Identify the parasite.
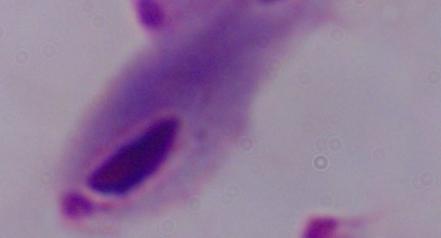
A trichomonad.

Captured at 1000x magnification. Photomicrograph.